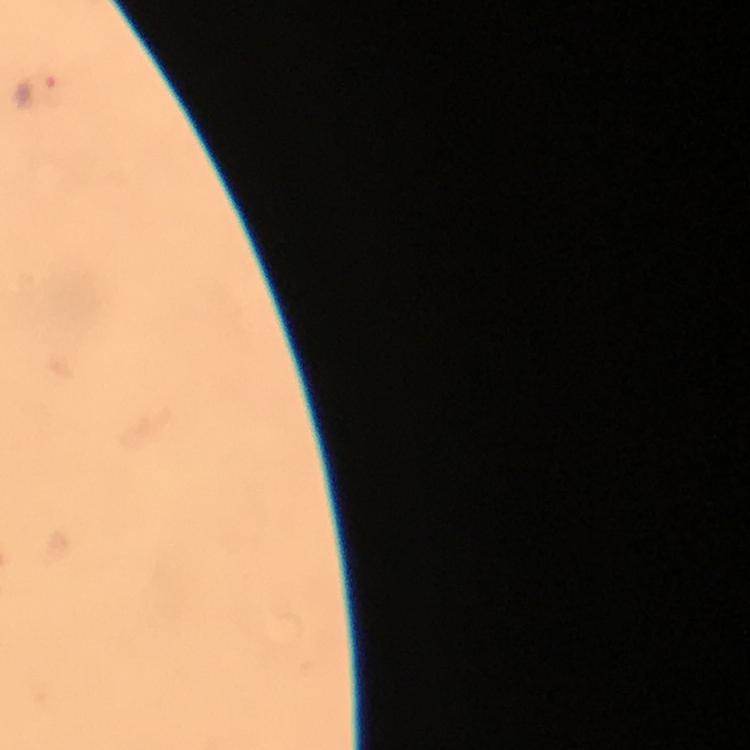 Approximate centers as (x, y) in pixels. Plasmodium parasite locations: (36, 95). At 100x magnification. Photographed with a smartphone mounted on the microscope. A crop from one field of view. From a malaria diagnostic workup. Giemsa-stained preparation. Thick blood film. Image is 750×750 pixels. Immersion oil was used.